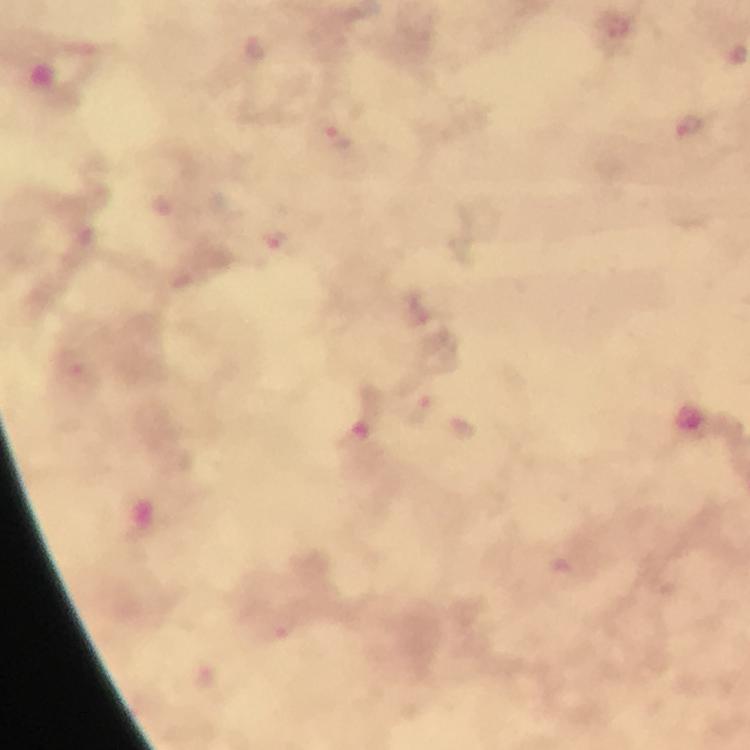
Approximate centers as (x, y) in pixels.
Summary:
  - Plasmodium parasite locations: (616, 26), (255, 46), (691, 127), (338, 138), (276, 240), (422, 306), (72, 363), (421, 410), (460, 428), (283, 622)
  - Stain: Giemsa
  - Immersion oil: applied
  - Capture: smartphone photograph through a microscope
  - Cropped from: one field of view
  - Magnification: 100x
  - Image size: 750×750 pixels
  - Context: from a diagnostic examination for malaria
  - Preparation: thick smear